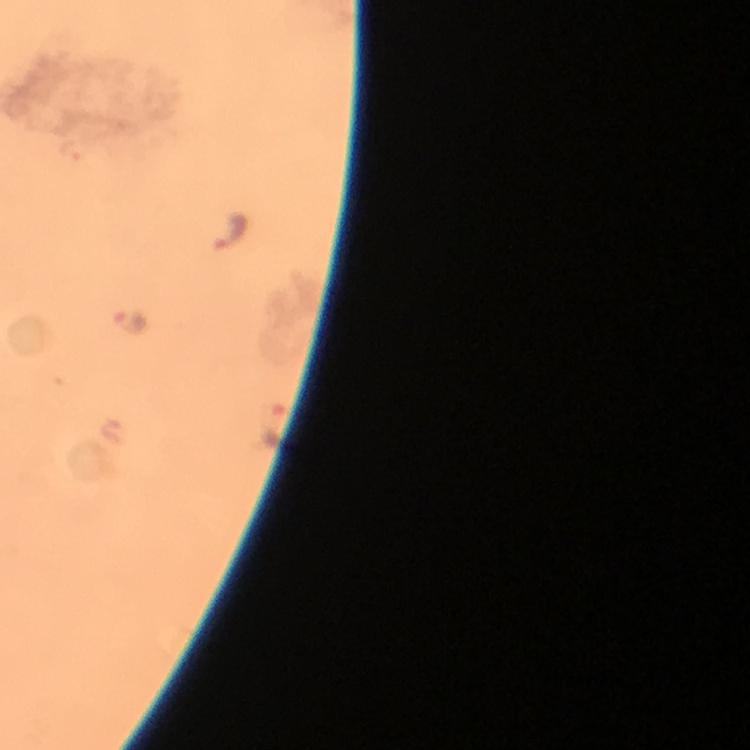

context = from a malaria diagnostic workup
capture = smartphone camera through the microscope
immersion oil = applied
Plasmodium parasite locations = approximate object centers, in pixels from the top-left corner: (x=229, y=230), (x=130, y=322), (x=274, y=425)
image size = 750×750 pixels
magnification = 100x
preparation = thick blood film
cropped from = a single field of view
stain = Giemsa